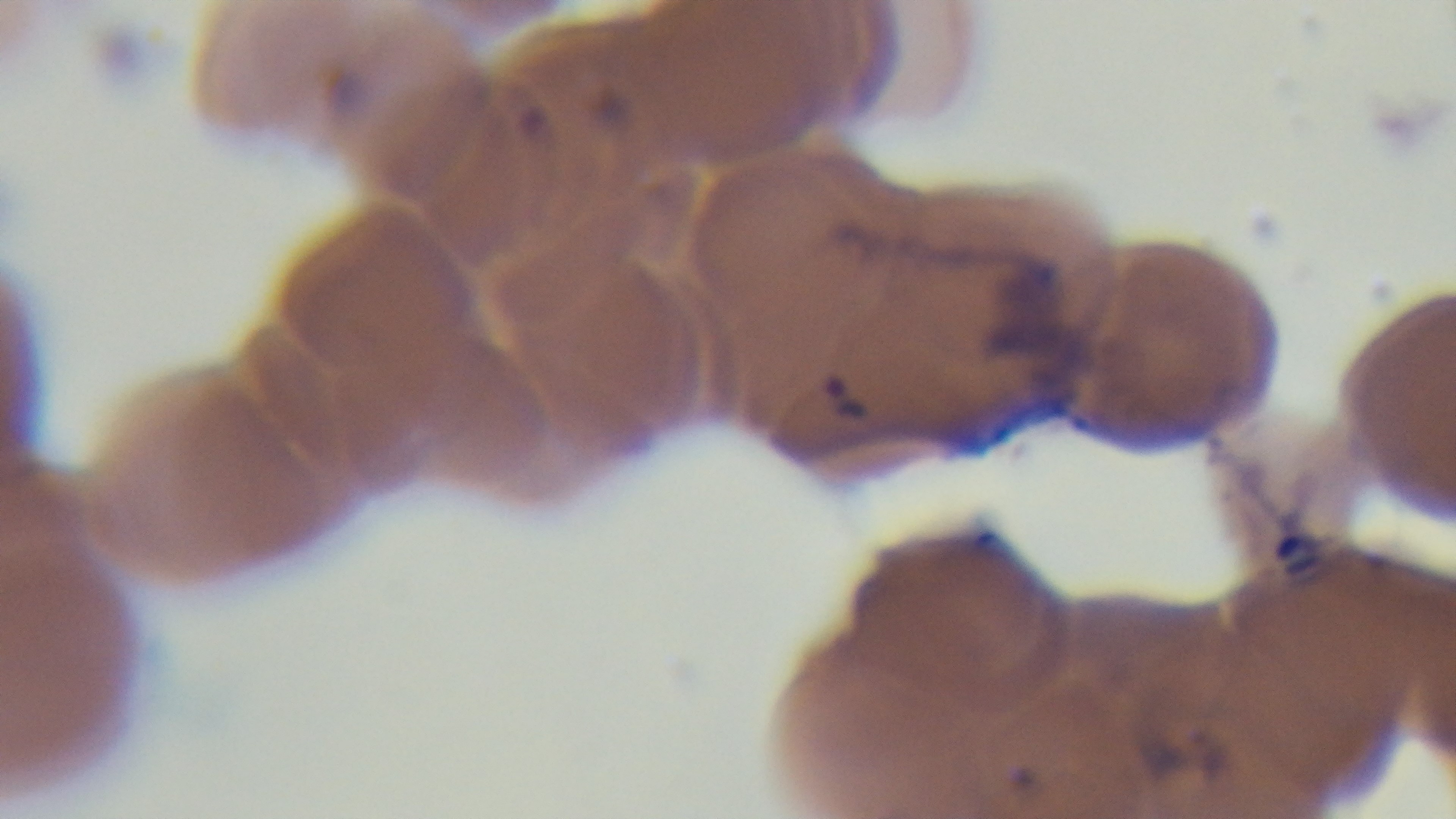

preparation: thin smear
capture: mounted 4K digital camera
stain: Giemsa
modality: light microscopy
objective: 100x oil immersion
field_of_view: single
malaria_status: infected